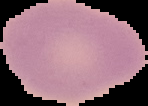

Summary:
  - Image size: 148×106 pixels
  - Preparation: thin blood film
  - Image type: segmented cell region on a black background
  - Malaria status: uninfected